Assess this cell for malaria.
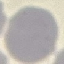

Uninfected.

Giemsa stain. Photographed with a smartphone camera at the microscope eyepiece. Thin blood film. Cell patch, automatically extracted from a larger field of view and resized to 64 × 64 pixels.